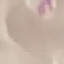
result: no malaria parasites seen
stain: Giemsa
image_type: automatically extracted cell patch, resized to 64 × 64 pixels
capture: smartphone through the microscope eyepiece
preparation: thin blood film